Describe the morphology of the red blood cells.
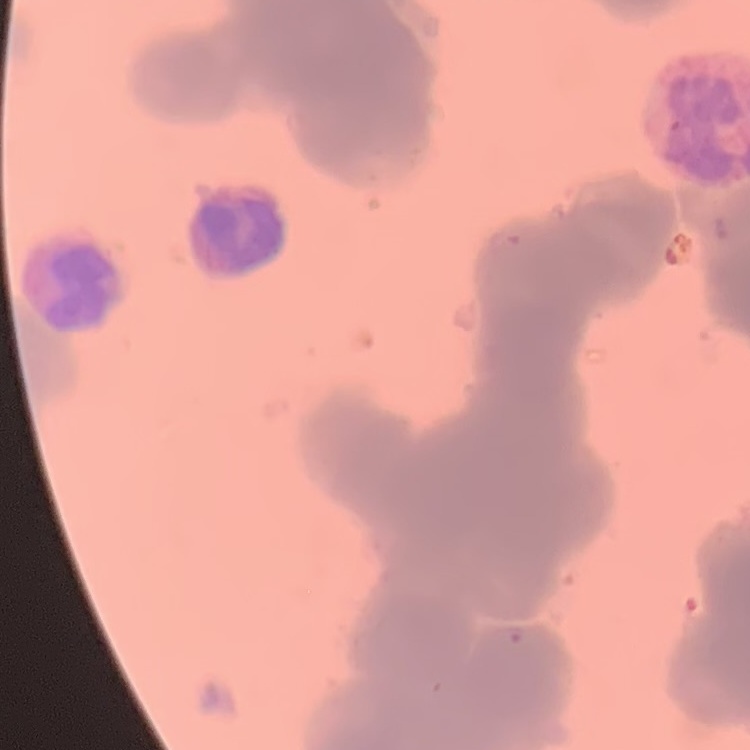

They show rouleaux formation.

One tile cut from a larger photomicrograph. Thin blood smear. Field's or Giemsa stain.